State which parasite is depicted.
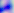

This is Toxoplasma gondii.

magnification: 400x
modality: micrograph